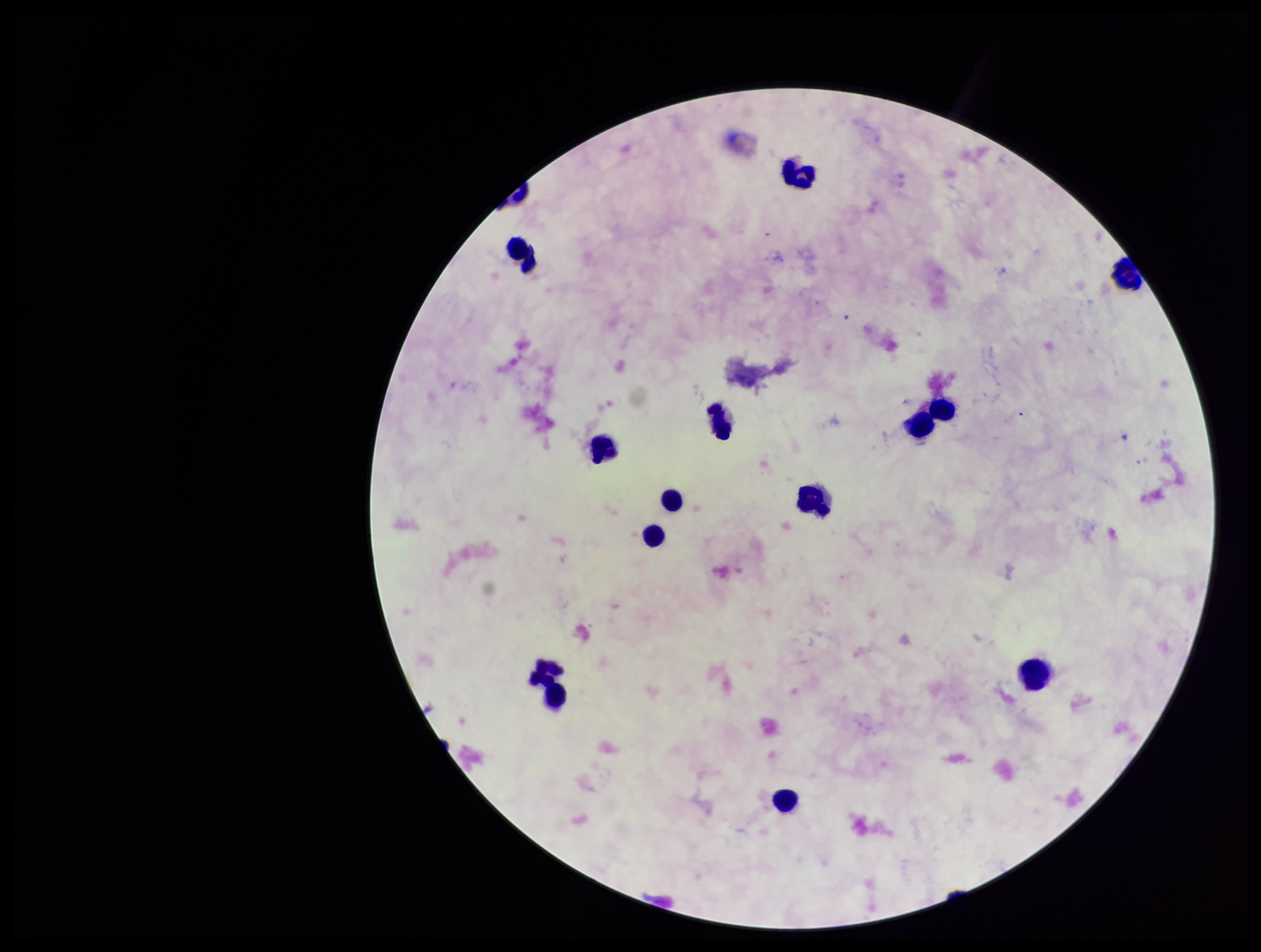

Single field of view. Leukocyte count: 12. Photographed through the microscope eyepiece with a smartphone camera. Image is 1261×952 pixels. Giemsa stain. Plasmodium parasites: none seen. Preparation: thick. Parasite count: 0. Patient malaria status: negative.